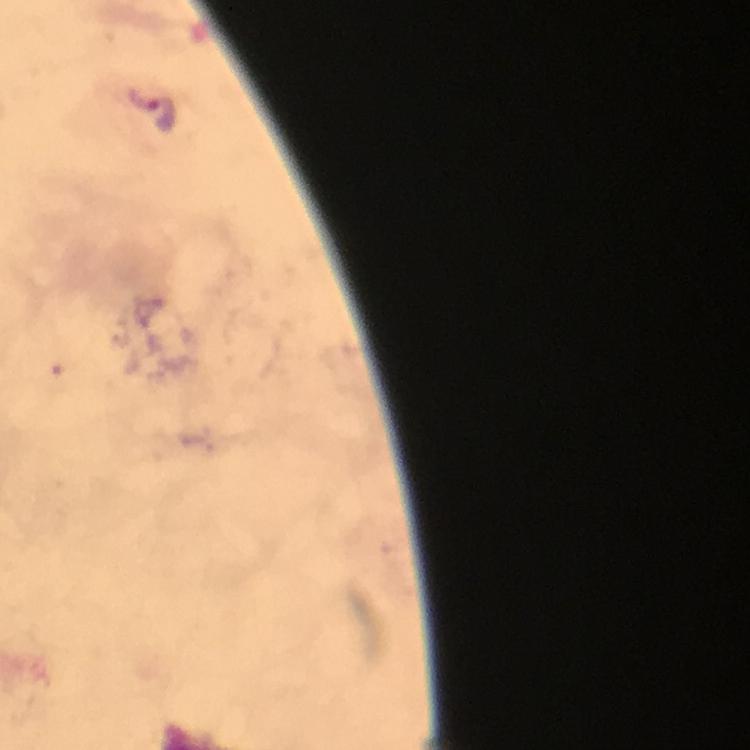 Approximate object centers, in pixels from the top-left corner. Plasmodium parasite locations: (x=161, y=121). Giemsa stain. Thick smear. From a malaria diagnostic workup. 100x magnification. Immersion oil was used. Image is 750×750 pixels. Smartphone photograph taken through a microscope. Cropped region of a single field of view.